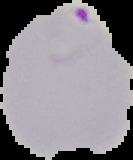
Summary:
  - Image type: segmented cell region on a black background
  - Result: malaria parasites identified
  - Image size: 133×160 pixels
  - Preparation: thin blood film